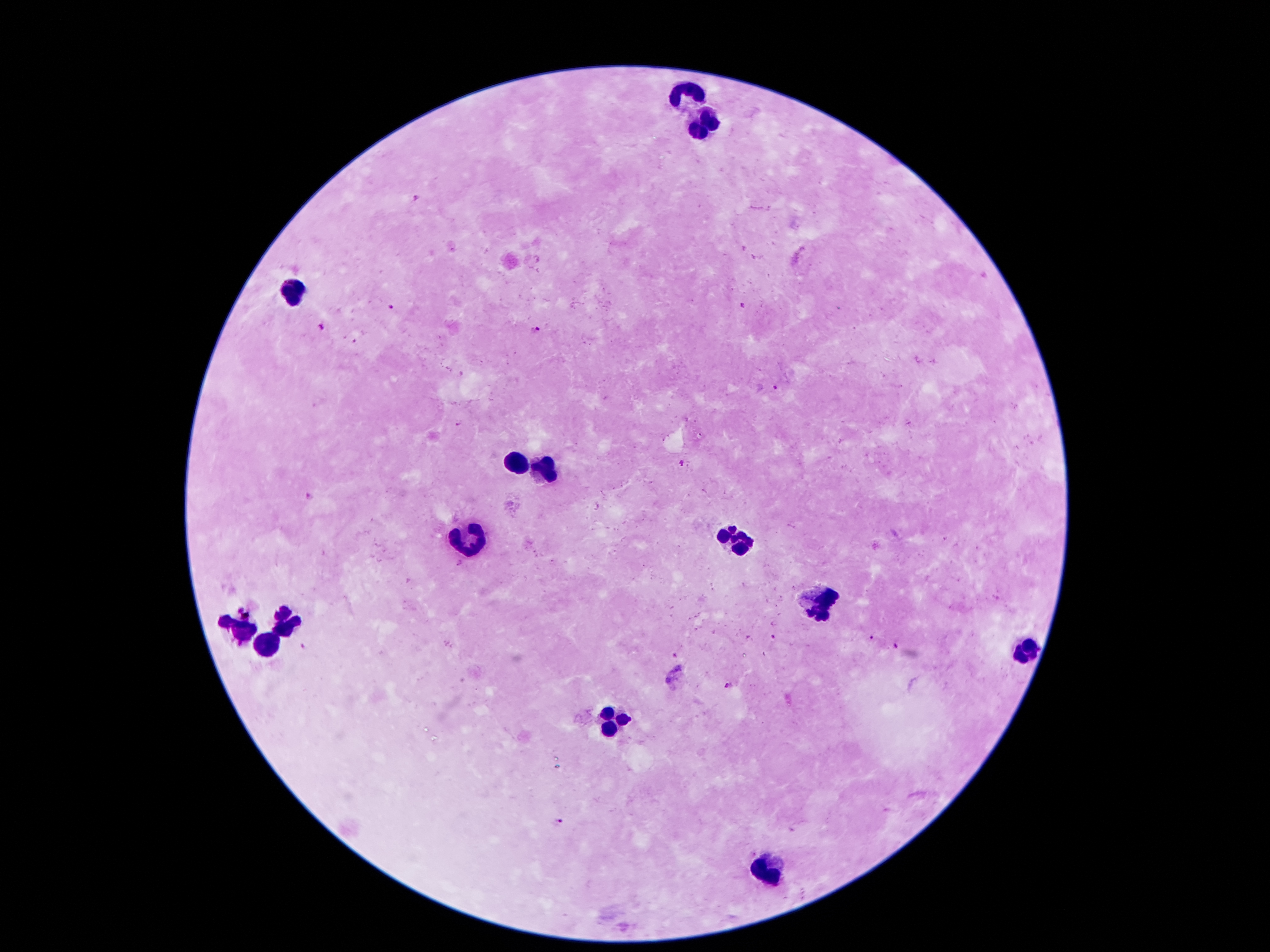

Approximate centers as [x, y] in pixels. Plasmodium parasite locations: [414, 197], [742, 305], [392, 307], [322, 324], [533, 331], [775, 388], [683, 464], [309, 496], [872, 639], [304, 646], [896, 646], [676, 656], [678, 668], [668, 680], [730, 685], [558, 821]. Leukocyte locations: [685, 90], [705, 129], [288, 294], [515, 463], [545, 470], [737, 539], [470, 542], [816, 603], [285, 625], [241, 631], [268, 641], [1024, 653], [612, 721], [771, 868]. 100x magnification. Photographed through the microscope eyepiece with a smartphone camera. Single field of view. Thick blood film. Patient malaria status: infected with Plasmodium falciparum. Giemsa stain. Image is 1270×952 pixels.